Classify this cell by malaria status.
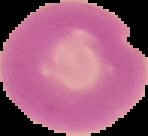
Uninfected.

image size = 148×136 pixels
preparation = thin blood smear
image type = segmented cell region on a black background